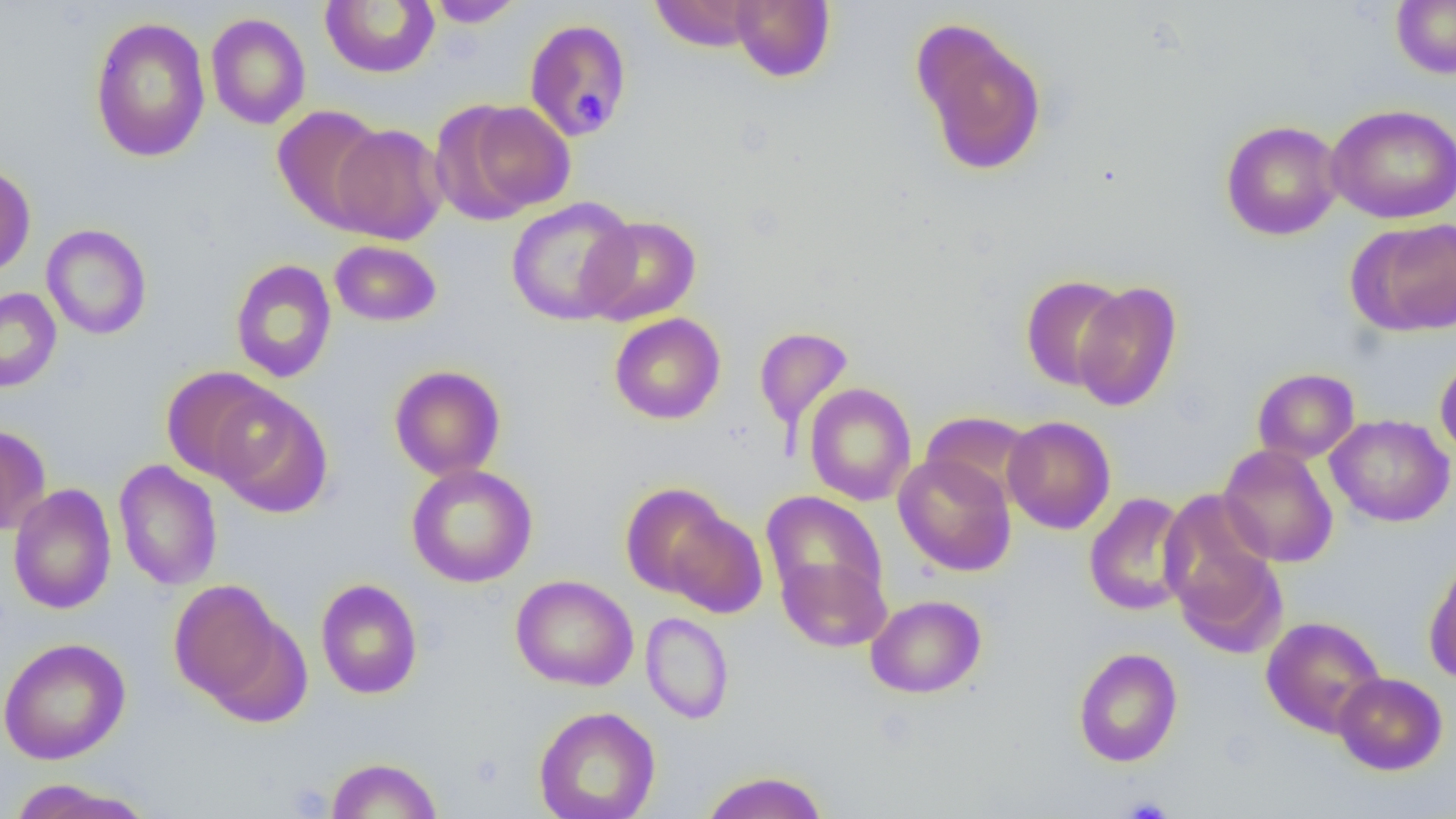
Summary:
  - Coordinate format: approximate bounding boxes as named x1/y1/x2/y2 corners in pixels
  - Uninfected red blood cell locations: (x1=320, y1=0, x2=440, y2=78), (x1=424, y1=0, x2=525, y2=28), (x1=649, y1=0, x2=763, y2=51), (x1=730, y1=0, x2=835, y2=83), (x1=1391, y1=0, x2=1456, y2=78), (x1=205, y1=12, x2=311, y2=129), (x1=89, y1=17, x2=211, y2=161), (x1=524, y1=18, x2=632, y2=141), (x1=910, y1=18, x2=1048, y2=176), (x1=441, y1=99, x2=576, y2=220), (x1=1326, y1=104, x2=1456, y2=224), (x1=273, y1=105, x2=389, y2=231), (x1=1220, y1=120, x2=1343, y2=241), (x1=330, y1=123, x2=449, y2=245), (x1=0, y1=163, x2=36, y2=278), (x1=505, y1=197, x2=639, y2=325), (x1=581, y1=216, x2=701, y2=325), (x1=1352, y1=219, x2=1456, y2=337), (x1=41, y1=224, x2=152, y2=340), (x1=329, y1=240, x2=442, y2=327), (x1=230, y1=258, x2=337, y2=384), (x1=1019, y1=274, x2=1129, y2=391), (x1=1072, y1=281, x2=1183, y2=412), (x1=0, y1=288, x2=62, y2=392), (x1=609, y1=312, x2=726, y2=425), (x1=753, y1=326, x2=853, y2=439), (x1=1435, y1=354, x2=1456, y2=463), (x1=389, y1=364, x2=506, y2=481), (x1=161, y1=366, x2=283, y2=483), (x1=1252, y1=368, x2=1360, y2=464), (x1=804, y1=383, x2=916, y2=506), (x1=209, y1=388, x2=333, y2=518), (x1=920, y1=411, x2=1036, y2=507), (x1=1325, y1=414, x2=1454, y2=527), (x1=1002, y1=415, x2=1116, y2=534), (x1=0, y1=425, x2=51, y2=535), (x1=1217, y1=444, x2=1338, y2=567), (x1=893, y1=452, x2=1016, y2=577), (x1=113, y1=459, x2=223, y2=591), (x1=406, y1=464, x2=538, y2=588), (x1=8, y1=483, x2=117, y2=615), (x1=620, y1=483, x2=735, y2=601), (x1=1160, y1=490, x2=1280, y2=635), (x1=761, y1=492, x2=887, y2=608), (x1=1083, y1=492, x2=1196, y2=616), (x1=664, y1=509, x2=768, y2=618), (x1=777, y1=554, x2=891, y2=652), (x1=1424, y1=557, x2=1456, y2=685), (x1=511, y1=574, x2=638, y2=691), (x1=315, y1=578, x2=423, y2=699), (x1=168, y1=579, x2=289, y2=707), (x1=865, y1=594, x2=986, y2=698), (x1=640, y1=612, x2=734, y2=724), (x1=1260, y1=616, x2=1387, y2=738), (x1=0, y1=637, x2=130, y2=764), (x1=1073, y1=647, x2=1183, y2=767), (x1=1333, y1=672, x2=1447, y2=775), (x1=533, y1=706, x2=661, y2=819), (x1=326, y1=757, x2=443, y2=818), (x1=700, y1=770, x2=829, y2=819), (x1=5, y1=779, x2=156, y2=819)
  - Platelet locations: (x1=571, y1=86, x2=615, y2=132), (x1=1119, y1=796, x2=1174, y2=819)
  - Slide-level diagnosis: negative for blood parasites
  - Image size: 1456×819 pixels
  - Field of view: one of a larger specimen
  - Magnification: 1000x
  - Modality: light microscopy
  - Preparation: thin blood film